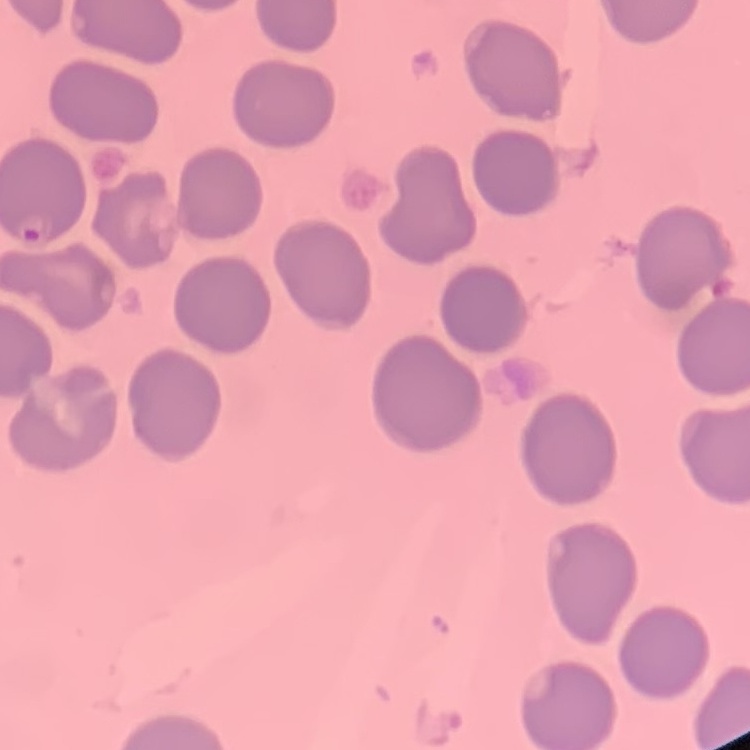

Summary:
  - Erythrocyte morphology: no rouleaux formation
  - Image type: square crop of a larger photomicrograph
  - Preparation: thin peripheral smear
  - Stain: Field's or Giemsa